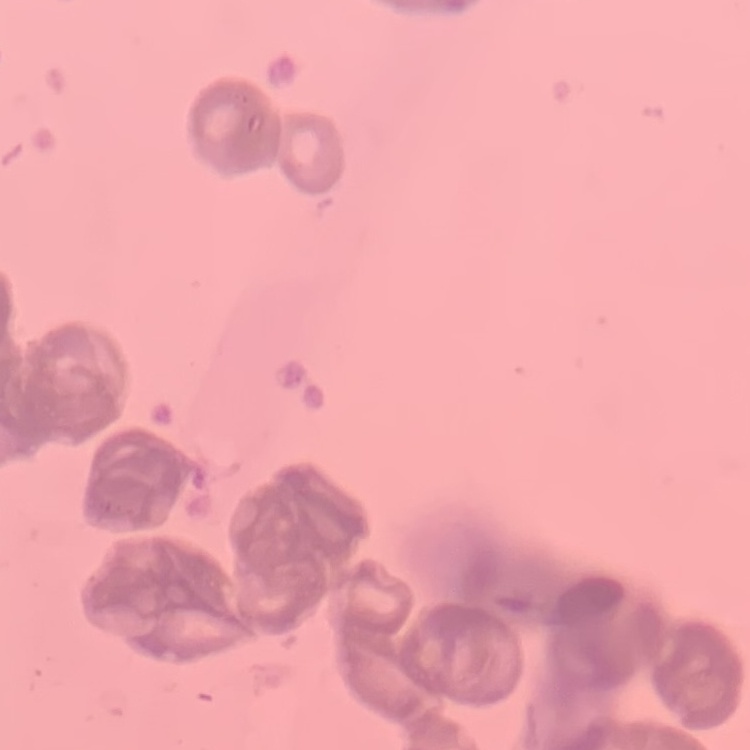

erythrocyte morphology = rouleaux formation
preparation = thin blood smear
image type = one tile cut from a larger photomicrograph
stain = Field's or Giemsa